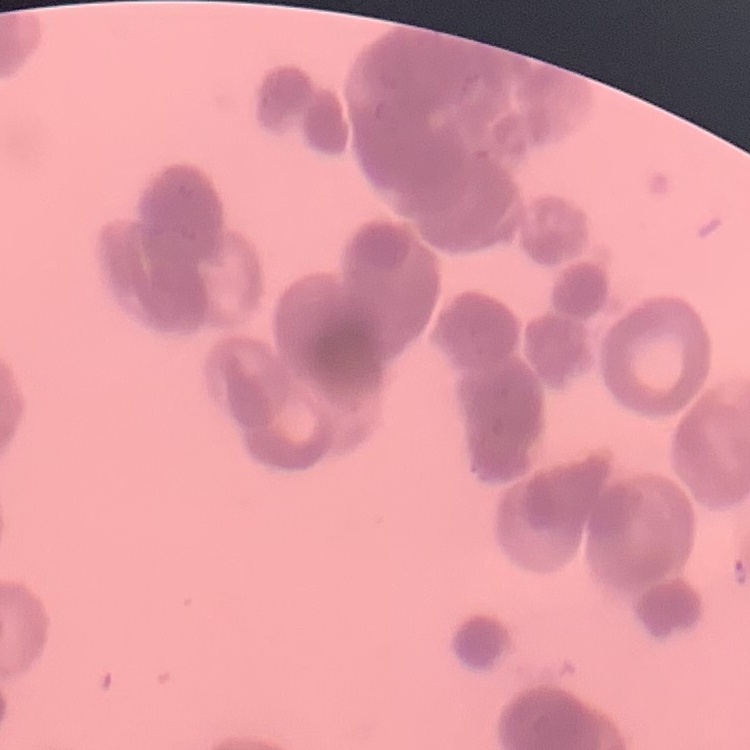
Summary:
  - Red blood cell morphology: rouleaux formation
  - Stain: Field's or Giemsa
  - Preparation: thin blood film
  - Image type: square crop of a larger photomicrograph